Report the malaria status of this cell.
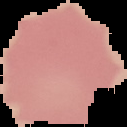
Uninfected.

Image is 127×127 pixels. Cell region segmented out of the field of view; the surrounding area is masked to black. From a thin blood smear.